Classify this cell by malaria status.
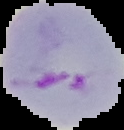
It is parasitized.

From a thin blood smear. Cell region segmented out of the field of view; the surrounding area is masked to black. Image is 124×130 pixels.